Outline each Plasmodium vivax-infected red blood cell.
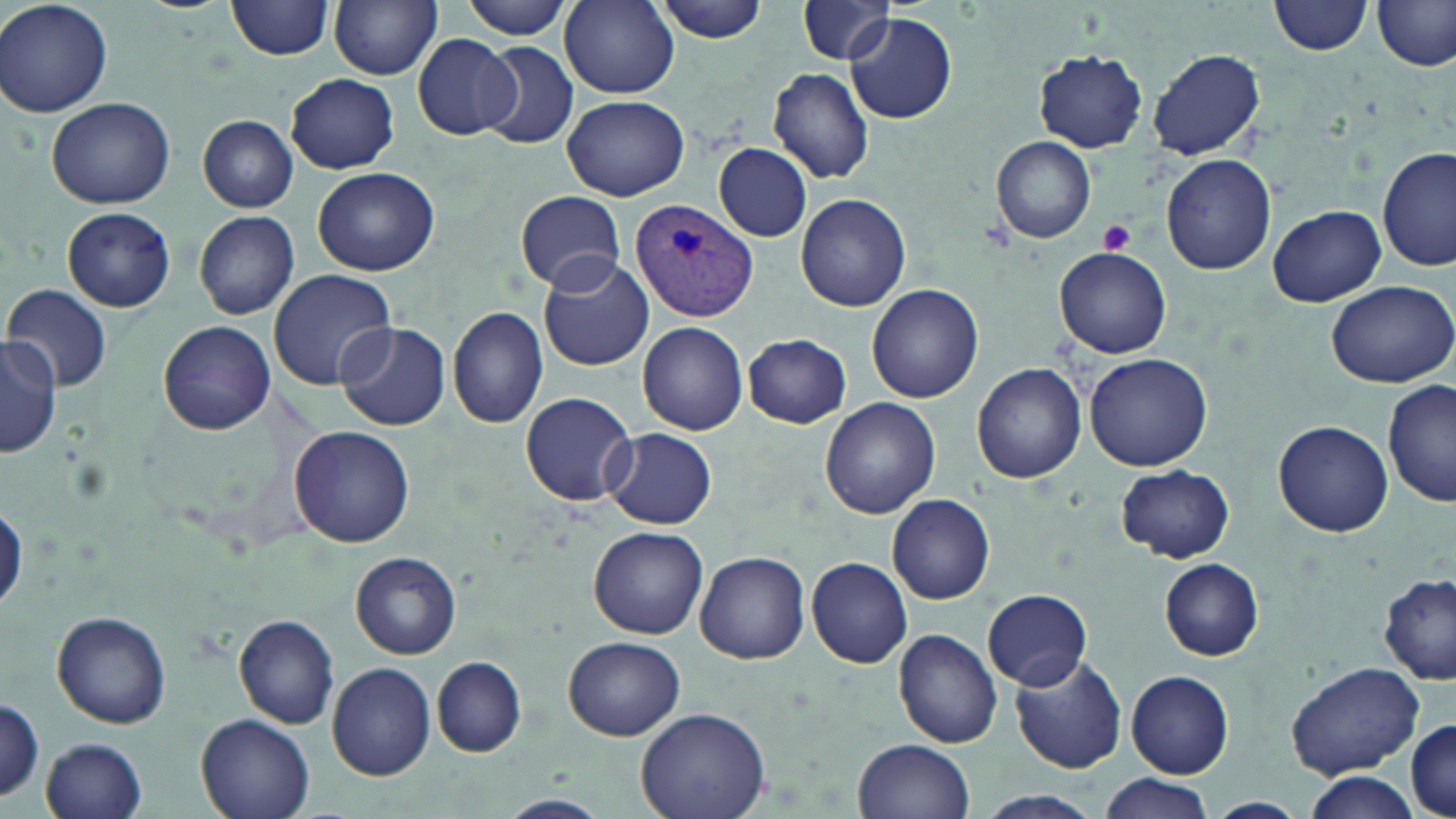
Approximate bounding boxes as named x1/y1/x2/y2 corners in pixels.
Plasmodium vivax-infected red blood cells: (x1=629, y1=198, x2=760, y2=322).

{
  "slide_level_diagnosis": "Plasmodium vivax",
  "image_size": "1456×819 pixels",
  "magnification": "1000x",
  "platelet_locations": "approximate bounding boxes as named x1/y1/x2/y2 corners in pixels: (x1=1098, y1=221, x2=1135, y2=254)",
  "field_of_view": "one of a larger specimen",
  "uninfected_red_blood_cell_locations": "approximate bounding boxes as named x1/y1/x2/y2 corners in pixels: (x1=1, y1=0, x2=114, y2=118), (x1=227, y1=0, x2=336, y2=59), (x1=329, y1=0, x2=442, y2=79), (x1=458, y1=0, x2=578, y2=39), (x1=650, y1=0, x2=772, y2=43), (x1=1269, y1=0, x2=1376, y2=57), (x1=1281, y1=0, x2=1456, y2=65), (x1=1373, y1=0, x2=1455, y2=72), (x1=559, y1=2, x2=679, y2=98), (x1=796, y1=3, x2=901, y2=67), (x1=845, y1=13, x2=956, y2=125), (x1=413, y1=34, x2=518, y2=141), (x1=475, y1=40, x2=578, y2=150), (x1=1149, y1=48, x2=1265, y2=161), (x1=1033, y1=50, x2=1148, y2=153), (x1=769, y1=67, x2=876, y2=184), (x1=286, y1=73, x2=399, y2=173), (x1=563, y1=94, x2=688, y2=200), (x1=46, y1=97, x2=175, y2=209), (x1=198, y1=115, x2=299, y2=211), (x1=992, y1=137, x2=1097, y2=243), (x1=714, y1=144, x2=811, y2=241), (x1=1379, y1=146, x2=1454, y2=271), (x1=1160, y1=153, x2=1278, y2=276), (x1=312, y1=166, x2=439, y2=276), (x1=515, y1=191, x2=625, y2=291), (x1=796, y1=193, x2=910, y2=312), (x1=1265, y1=204, x2=1384, y2=307), (x1=62, y1=206, x2=175, y2=311), (x1=193, y1=210, x2=300, y2=319), (x1=1055, y1=246, x2=1172, y2=358), (x1=536, y1=251, x2=653, y2=369), (x1=268, y1=270, x2=396, y2=391), (x1=1324, y1=278, x2=1456, y2=388), (x1=867, y1=283, x2=983, y2=403), (x1=6, y1=286, x2=113, y2=389), (x1=448, y1=305, x2=549, y2=428), (x1=159, y1=320, x2=276, y2=435), (x1=336, y1=320, x2=450, y2=430), (x1=638, y1=321, x2=749, y2=434), (x1=744, y1=333, x2=852, y2=428), (x1=1, y1=337, x2=63, y2=457), (x1=1085, y1=353, x2=1212, y2=471), (x1=972, y1=363, x2=1086, y2=483), (x1=1383, y1=380, x2=1455, y2=508), (x1=520, y1=390, x2=637, y2=506), (x1=819, y1=397, x2=940, y2=519), (x1=1272, y1=419, x2=1393, y2=536), (x1=291, y1=425, x2=415, y2=547), (x1=603, y1=427, x2=718, y2=530), (x1=1114, y1=464, x2=1235, y2=562), (x1=886, y1=494, x2=995, y2=604), (x1=1, y1=501, x2=26, y2=616), (x1=588, y1=526, x2=707, y2=639), (x1=695, y1=549, x2=810, y2=664), (x1=351, y1=552, x2=460, y2=657), (x1=807, y1=557, x2=913, y2=668), (x1=1157, y1=558, x2=1264, y2=660), (x1=1376, y1=575, x2=1456, y2=684), (x1=982, y1=588, x2=1093, y2=690), (x1=51, y1=610, x2=172, y2=728), (x1=234, y1=615, x2=340, y2=728), (x1=892, y1=628, x2=1003, y2=749), (x1=564, y1=636, x2=684, y2=741), (x1=1008, y1=652, x2=1128, y2=773), (x1=431, y1=656, x2=526, y2=757), (x1=1285, y1=661, x2=1426, y2=781), (x1=328, y1=662, x2=435, y2=779), (x1=1126, y1=670, x2=1234, y2=778), (x1=0, y1=697, x2=44, y2=803), (x1=636, y1=706, x2=769, y2=819), (x1=195, y1=714, x2=316, y2=819), (x1=1407, y1=717, x2=1455, y2=819), (x1=41, y1=737, x2=147, y2=818), (x1=854, y1=738, x2=974, y2=819), (x1=1298, y1=770, x2=1425, y2=819), (x1=1097, y1=776, x2=1218, y2=819), (x1=965, y1=791, x2=1109, y2=819), (x1=501, y1=793, x2=608, y2=817), (x1=1201, y1=797, x2=1308, y2=818)",
  "modality": "optical microscopy",
  "stain": "May-Grünwald-Giemsa",
  "preparation": "thin blood smear"
}